Classify this cell by malaria status.
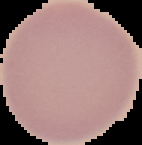

It is uninfected.

From a thin blood smear. Image is 142×145 pixels. The area outside the segmented cell region is set to black.